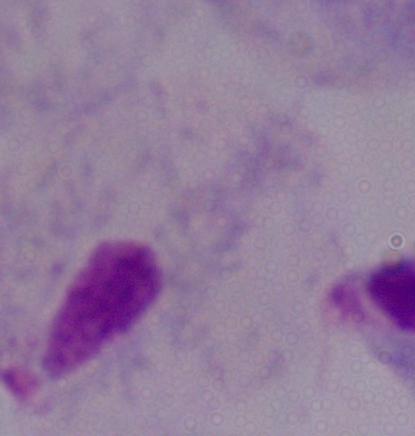

Summary:
  - Identification: trichomonad
  - Magnification: 1000x
  - Modality: micrograph